Classify this cell by malaria status.
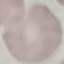

It is uninfected.

Summary:
  - Preparation: thin blood smear
  - Capture: smartphone through the microscope eyepiece
  - Stain: Giemsa
  - Image type: cell patch, automatically extracted from a larger field of view and resized to 64 × 64 pixels